Assess this cell for malaria.
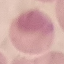

It is uninfected.

Summary:
  - Image type: cell patch, automatically extracted from a larger field of view and resized to 64 × 64 pixels
  - Capture: smartphone camera at the microscope eyepiece
  - Stain: Giemsa
  - Preparation: thin smear